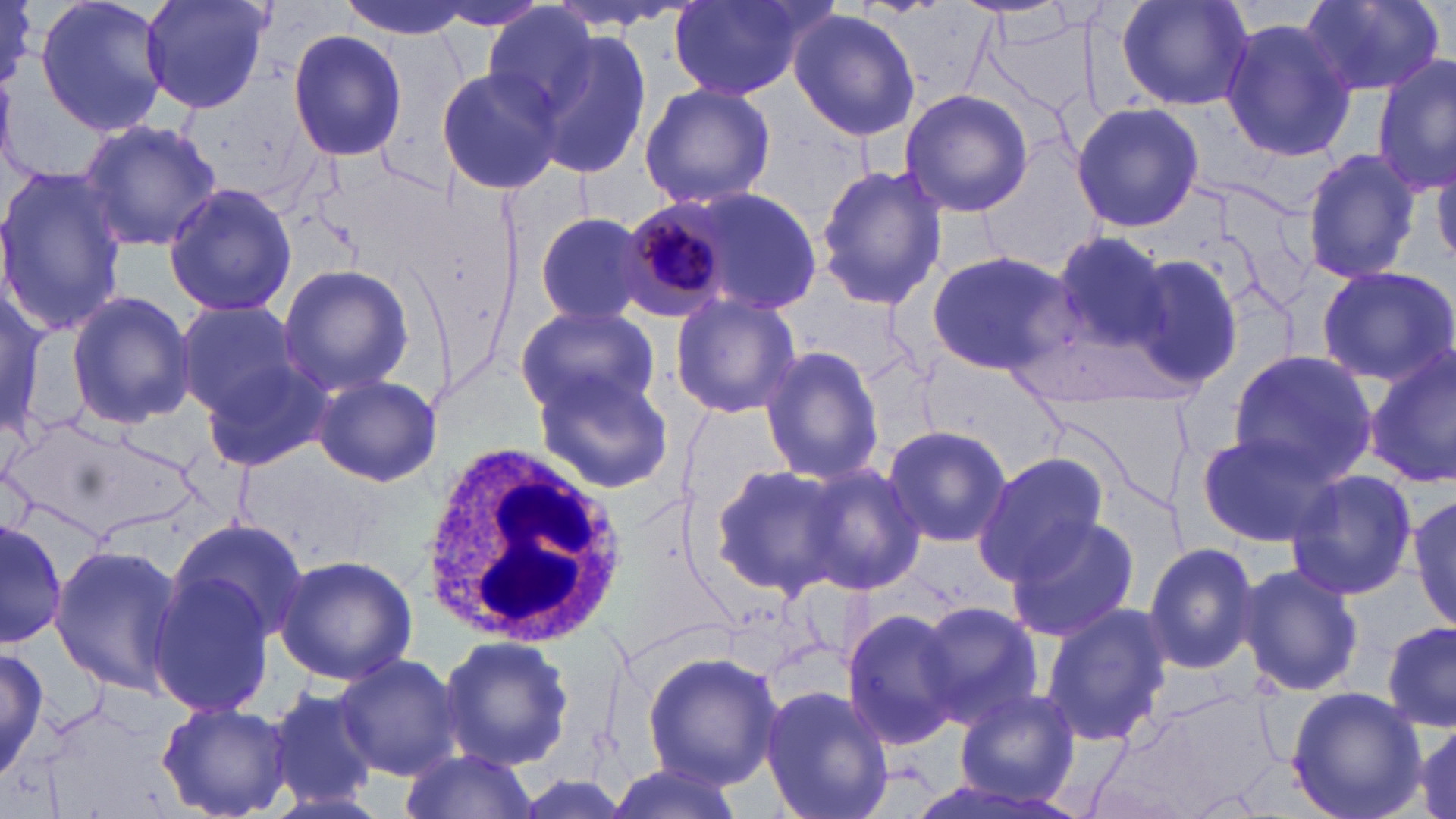
Summary:
  - Coordinate format: approximate bounding boxes as (x1,y1)-(x2,y2) corner pairs in pixels
  - White blood cell locations: (417,437)-(625,645)
  - Plasmodium malariae-infected red blood cell locations: (617,197)-(734,320)
  - Uninfected red blood cell locations: (0,0)-(34,88), (35,0)-(168,137), (141,0)-(272,115), (337,0)-(476,39), (1116,0)-(1255,112), (1299,0)-(1443,97), (668,1)-(814,99), (424,3)-(557,33), (479,3)-(600,122), (787,8)-(922,140), (1217,17)-(1357,164), (287,28)-(407,163), (528,30)-(654,179), (1373,56)-(1456,195), (435,66)-(563,198), (639,82)-(775,210), (899,89)-(1033,217), (1070,101)-(1204,232), (78,120)-(224,250), (1299,146)-(1424,286), (1433,159)-(1455,267), (815,164)-(948,309), (0,166)-(129,334), (161,182)-(298,321), (704,189)-(820,317), (533,211)-(659,325), (1046,229)-(1174,361), (925,249)-(1078,377), (1121,249)-(1244,392), (276,264)-(415,396), (1314,264)-(1455,387), (63,289)-(195,431), (0,291)-(52,439), (669,292)-(802,420), (174,298)-(307,421), (515,302)-(658,419), (759,346)-(884,485), (1365,349)-(1455,492), (1226,350)-(1376,488), (199,361)-(333,470), (530,364)-(675,494), (309,374)-(441,487), (881,423)-(1010,546), (1194,431)-(1339,548), (975,450)-(1108,581), (796,461)-(926,595), (711,462)-(851,597), (1284,468)-(1418,601), (1409,493)-(1456,630), (1003,515)-(1140,644), (164,517)-(309,652), (0,518)-(65,647), (1143,539)-(1261,677), (50,546)-(184,695), (275,554)-(418,686), (1238,562)-(1363,698), (146,567)-(280,718), (913,600)-(1042,725), (1040,604)-(1173,749), (841,605)-(962,748), (1382,621)-(1456,735), (437,634)-(573,771), (2,644)-(49,783), (642,650)-(781,789), (334,653)-(461,779), (759,684)-(894,819), (1097,685)-(1282,819), (949,686)-(1085,807), (1284,686)-(1428,819), (267,687)-(379,811), (156,702)-(294,819), (1409,720)-(1455,819), (397,748)-(538,819), (605,766)-(745,819)
  - Slide-level diagnosis: Plasmodium malariae
  - Magnification: 1000x
  - Image size: 1456×819 pixels
  - Field of view: one of a larger specimen
  - Stain: May-Grünwald-Giemsa
  - Modality: optical microscopy
  - Preparation: thin blood smear